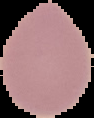
Summary:
  - Result: no Plasmodium parasites seen
  - Image size: 94×118 pixels
  - Preparation: thin blood smear
  - Image type: segmented cell region on a black background